Give the extent of all Plasmodium vivax-infected red blood cells.
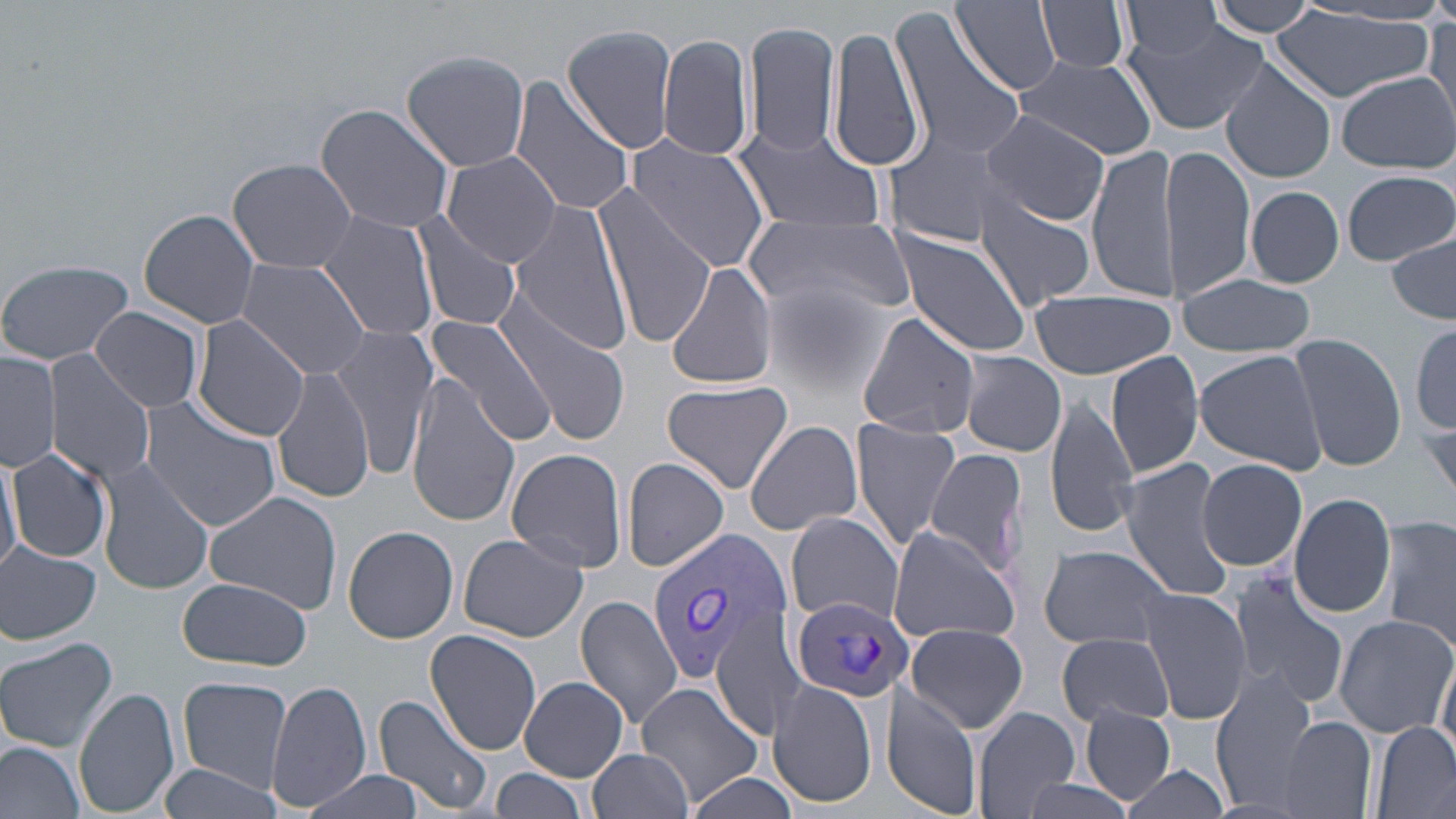

Approximate bounding boxes as [x1, y1, x2, y2] in pixels.
Plasmodium vivax-infected red blood cells: [646, 527, 793, 682], [789, 594, 912, 704].

Summary:
  - Uninfected red blood cell locations: [953, 0, 1062, 94], [1037, 0, 1131, 74], [1205, 1, 1322, 37], [1122, 4, 1225, 60], [1273, 9, 1433, 103], [887, 10, 1026, 161], [1426, 17, 1456, 128], [744, 18, 840, 160], [1122, 19, 1269, 133], [828, 21, 929, 175], [562, 24, 680, 155], [658, 32, 755, 163], [400, 49, 531, 172], [1014, 56, 1158, 159], [1220, 60, 1336, 183], [1336, 72, 1455, 173], [509, 78, 637, 218], [315, 102, 457, 236], [983, 110, 1108, 226], [729, 123, 886, 233], [879, 126, 1019, 249], [623, 134, 775, 273], [1086, 144, 1182, 302], [1160, 146, 1257, 300], [443, 151, 563, 269], [228, 157, 357, 273], [1341, 170, 1453, 266], [1244, 183, 1449, 280], [1246, 186, 1343, 287], [973, 193, 1097, 311], [597, 194, 719, 347], [509, 198, 633, 357], [138, 207, 262, 330], [315, 209, 441, 344], [412, 211, 524, 335], [747, 217, 913, 324], [889, 229, 1034, 357], [1387, 232, 1455, 325], [233, 258, 373, 382], [0, 259, 135, 365], [665, 260, 778, 391], [1173, 273, 1319, 358], [758, 278, 888, 399], [1027, 287, 1177, 379], [494, 296, 632, 445], [90, 306, 205, 414], [855, 311, 980, 440], [421, 317, 557, 447], [190, 318, 310, 443], [328, 324, 439, 476], [1412, 325, 1455, 437], [1285, 334, 1408, 471], [0, 348, 60, 473], [1193, 350, 1328, 474], [958, 351, 1065, 457], [43, 352, 157, 487], [1106, 352, 1204, 479], [272, 366, 374, 503], [1062, 366, 1194, 519], [404, 376, 519, 529], [662, 378, 794, 494], [1045, 393, 1141, 539], [141, 400, 281, 532], [1420, 407, 1455, 509], [850, 416, 961, 551], [744, 420, 863, 537], [6, 445, 113, 563], [0, 447, 20, 577], [506, 447, 629, 572], [922, 448, 1028, 578], [93, 455, 214, 594], [621, 457, 731, 571], [1196, 459, 1307, 570], [1120, 460, 1235, 602], [202, 490, 343, 615], [1287, 493, 1397, 617], [1379, 513, 1456, 654], [786, 514, 904, 628], [885, 525, 1023, 646], [342, 526, 459, 644], [456, 532, 588, 641], [0, 542, 102, 643], [1040, 544, 1172, 649], [1226, 570, 1349, 706], [173, 576, 315, 670], [1135, 588, 1251, 724], [575, 594, 686, 729], [709, 606, 808, 741], [1331, 612, 1456, 739], [904, 621, 1029, 733], [426, 629, 543, 756], [1057, 632, 1174, 726], [0, 635, 117, 754], [1434, 644, 1456, 763], [1209, 672, 1319, 815], [178, 677, 292, 792], [519, 677, 629, 781], [636, 680, 766, 808], [768, 680, 878, 809], [268, 682, 370, 813], [75, 686, 180, 817], [880, 686, 979, 815], [373, 693, 496, 816], [971, 706, 1081, 819], [1079, 707, 1177, 805], [1278, 717, 1376, 819], [1373, 720, 1455, 818], [0, 740, 86, 819], [589, 748, 695, 819], [155, 761, 288, 819], [1121, 764, 1233, 817], [491, 767, 591, 815], [302, 772, 427, 819], [684, 772, 802, 819], [1001, 777, 1145, 819]
  - Slide-level diagnosis: Plasmodium vivax
  - Modality: optical microscopy
  - Stain: May-Grünwald-Giemsa
  - Image size: 1456×819 pixels
  - Field of view: single
  - Preparation: thin blood smear
  - Magnification: 1000x